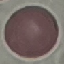
result = no malaria parasites detected
capture = smartphone through the microscope eyepiece
image type = automatically extracted cell patch, resized to 64 × 64 pixels
stain = Giemsa
preparation = thin blood smear